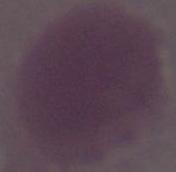
{
  "modality": "photomicrograph",
  "identification": "red blood cell",
  "magnification": "1000x"
}